State the blood parasite species.
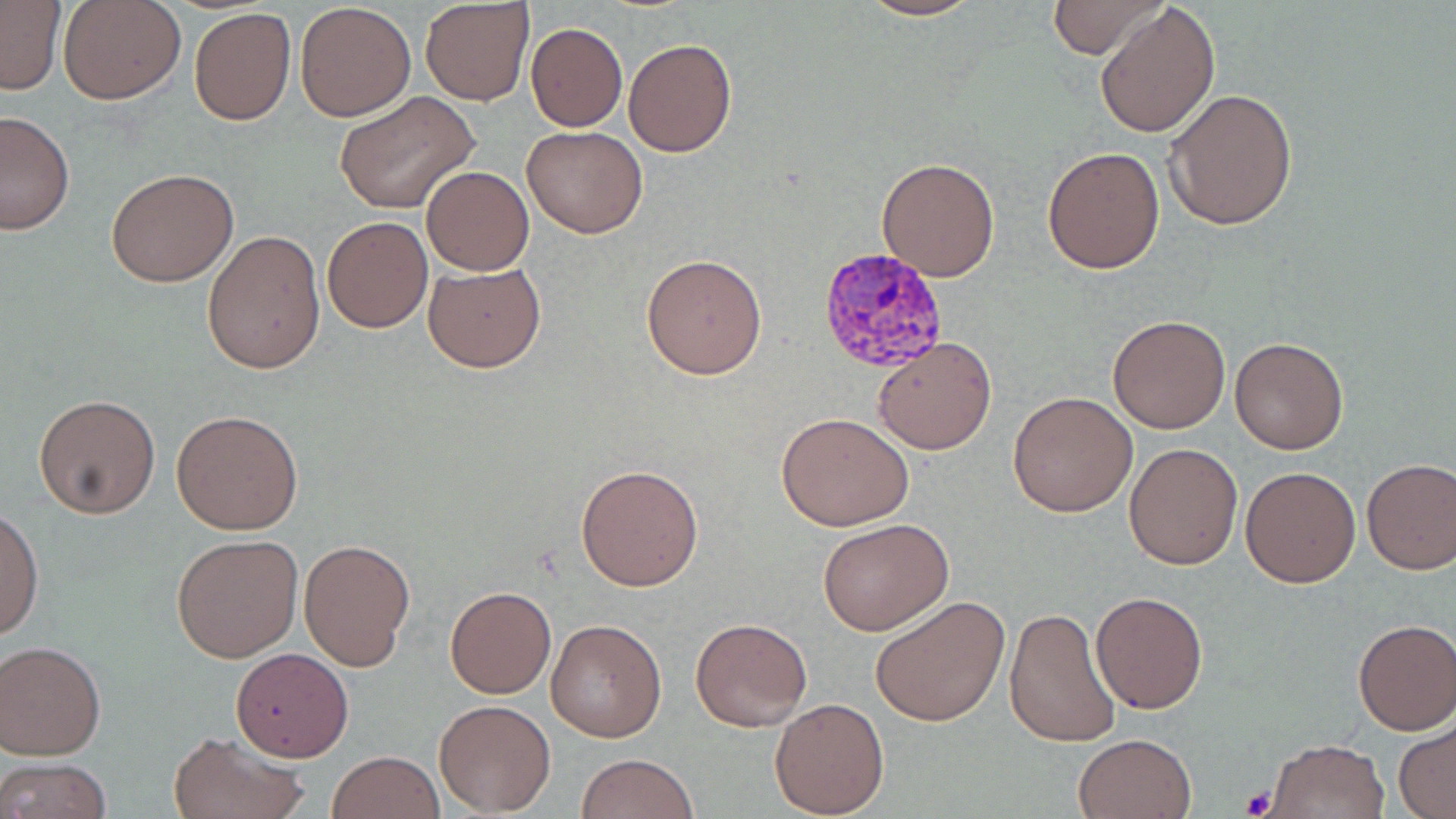
Plasmodium vivax.

Approximate bounding boxes as (x1,y1)-(x2,y2) corner pairs in pixels. Plasmodium vivax-infected red blood cell locations: (818,246)-(949,372). Uninfected red blood cell locations: (60,0)-(183,104), (420,0)-(536,105), (854,0)-(988,22), (1047,0)-(1168,59), (0,2)-(64,93), (295,2)-(417,120), (1095,3)-(1221,139), (188,8)-(297,126), (526,23)-(627,131), (624,37)-(737,157), (1161,88)-(1299,232), (334,91)-(481,215), (0,110)-(75,236), (522,125)-(647,238), (1042,146)-(1165,275), (877,156)-(1001,282), (421,166)-(534,275), (106,168)-(239,287), (321,215)-(433,333), (202,230)-(326,376), (641,252)-(767,378), (422,262)-(546,372), (1108,313)-(1230,432), (872,335)-(999,456), (1229,336)-(1350,455), (1008,390)-(1137,517), (34,393)-(163,520), (171,408)-(304,535), (776,412)-(915,531), (1124,442)-(1243,571), (1361,459)-(1456,575), (576,463)-(705,592), (1241,465)-(1362,588), (0,503)-(43,642), (818,519)-(953,636), (172,533)-(303,663), (298,538)-(415,670), (444,586)-(557,699), (1090,591)-(1209,714), (869,594)-(1010,727), (1004,606)-(1121,748), (690,616)-(813,732), (545,618)-(666,742), (1352,618)-(1456,735), (1,641)-(105,759), (230,648)-(353,762), (770,697)-(890,817), (433,698)-(556,816), (1394,721)-(1456,817), (168,730)-(309,819), (1073,731)-(1197,819), (1263,737)-(1389,817), (326,750)-(445,819), (577,753)-(698,819), (1,756)-(112,819). Platelet locations: (1240,786)-(1278,816). Image is 1456×819 pixels. Captured at 1000x magnification. Thin blood smear. One field of a larger specimen. May-Grünwald-Giemsa stain. Light microscopy.